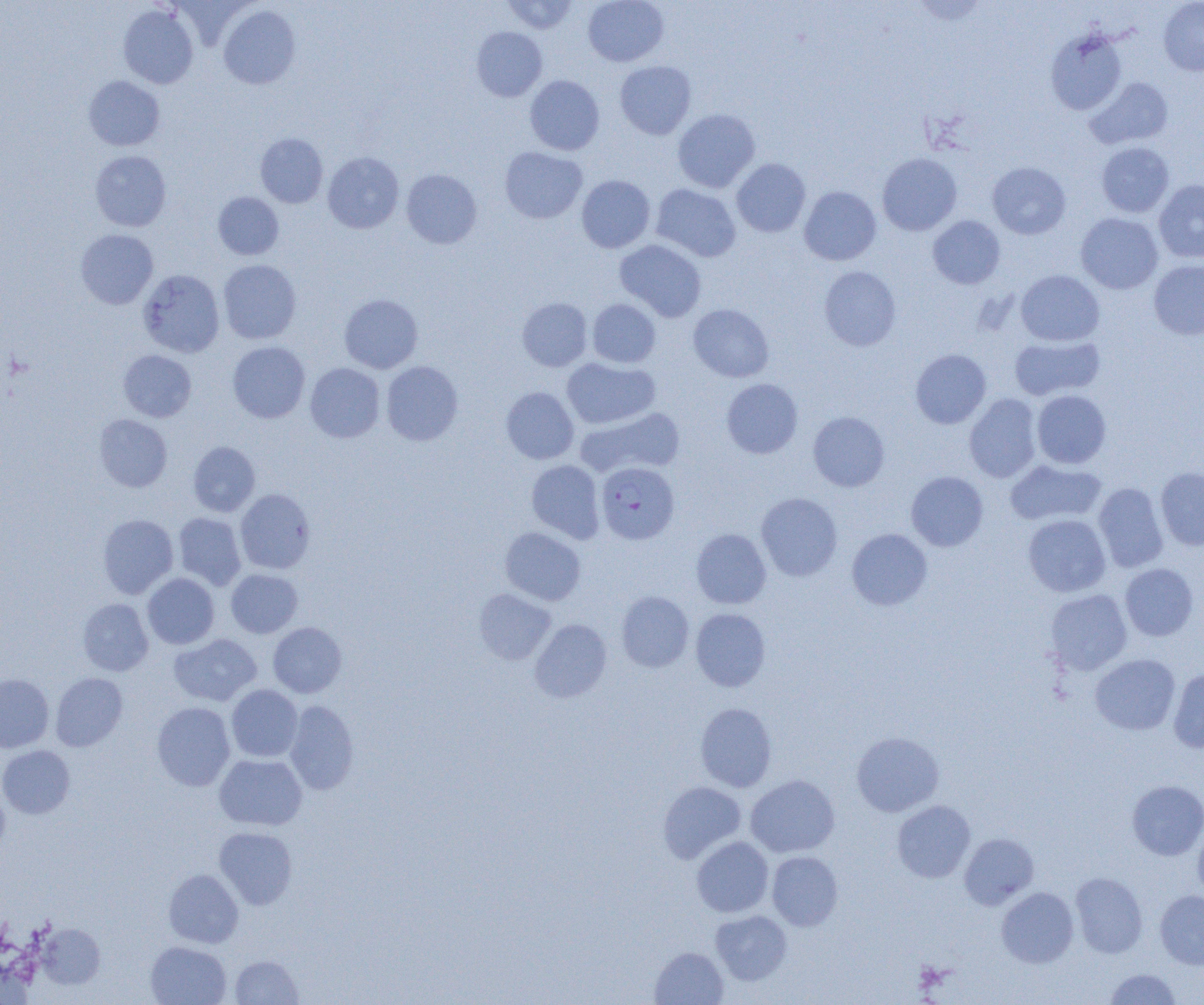

Summary:
  - Coordinate format: approximate bounding boxes as [x1, y1, x2, y2] in pixels
  - Plasmodium falciparum-infected red blood cell locations: [596, 462, 679, 544]
  - Uninfected red blood cell locations: [502, 0, 579, 34], [583, 0, 669, 67], [1158, 1, 1204, 76], [118, 5, 198, 89], [218, 5, 301, 89], [472, 26, 547, 101], [1045, 30, 1127, 115], [614, 61, 696, 140], [84, 75, 165, 151], [525, 75, 604, 155], [1086, 77, 1173, 149], [673, 108, 760, 193], [256, 133, 328, 208], [1096, 142, 1175, 218], [500, 147, 587, 223], [90, 150, 172, 231], [323, 152, 404, 233], [877, 153, 962, 235], [732, 158, 810, 237], [987, 162, 1070, 239], [402, 169, 482, 249], [577, 175, 655, 253], [1153, 180, 1204, 263], [651, 184, 741, 262], [799, 186, 881, 265], [213, 191, 284, 260], [1076, 213, 1163, 294], [928, 215, 1005, 289], [75, 229, 158, 309], [614, 239, 707, 322], [218, 259, 301, 344], [1148, 259, 1204, 340], [819, 266, 901, 351], [139, 269, 225, 357], [1016, 270, 1104, 346], [339, 294, 423, 373], [517, 297, 592, 371], [588, 299, 660, 368], [688, 304, 774, 382], [1010, 335, 1105, 400], [228, 341, 310, 423], [910, 349, 991, 428], [118, 350, 196, 422], [562, 357, 660, 429], [381, 361, 463, 445], [305, 363, 385, 442], [721, 378, 803, 458], [500, 387, 579, 464], [1032, 390, 1111, 468], [964, 393, 1042, 482], [576, 407, 684, 479], [808, 411, 889, 491], [94, 414, 172, 492], [188, 441, 260, 516], [1005, 459, 1106, 526], [526, 460, 605, 543], [1155, 466, 1204, 550], [906, 471, 988, 551], [1093, 483, 1169, 572], [235, 489, 315, 574], [756, 493, 843, 581], [173, 512, 246, 590], [97, 514, 178, 598], [1023, 514, 1111, 597], [500, 527, 586, 605], [691, 528, 771, 609], [847, 528, 932, 610], [1120, 563, 1199, 641], [226, 569, 303, 638], [142, 573, 219, 649], [474, 588, 556, 665], [1045, 589, 1132, 675], [616, 591, 694, 672], [77, 598, 153, 676], [691, 608, 770, 691], [530, 619, 612, 702], [268, 622, 347, 698], [169, 634, 262, 706], [1090, 654, 1180, 735], [1169, 669, 1204, 753], [0, 673, 54, 752], [51, 673, 128, 751], [226, 684, 303, 761], [284, 700, 359, 794], [152, 702, 235, 791], [695, 703, 777, 792], [851, 731, 944, 817], [0, 745, 75, 818], [214, 753, 307, 830], [746, 775, 840, 857], [1127, 780, 1204, 860], [657, 781, 746, 863], [0, 788, 9, 856], [892, 800, 975, 882], [1193, 821, 1204, 902], [214, 827, 297, 909], [959, 833, 1039, 909], [691, 837, 773, 917], [767, 851, 843, 930], [163, 869, 243, 948], [1070, 872, 1148, 958], [996, 887, 1079, 968], [1155, 890, 1204, 969], [710, 910, 792, 985], [37, 923, 105, 988], [145, 941, 232, 1005], [650, 946, 728, 1004], [230, 954, 303, 1004], [1104, 968, 1181, 1004]
  - Slide-level diagnosis: Plasmodium falciparum
  - Magnification: 1000x
  - Field of view: one of a larger specimen
  - Preparation: thin blood smear
  - Image size: 1204×1005 pixels
  - Modality: light microscopy